Identify the blood parasite species.
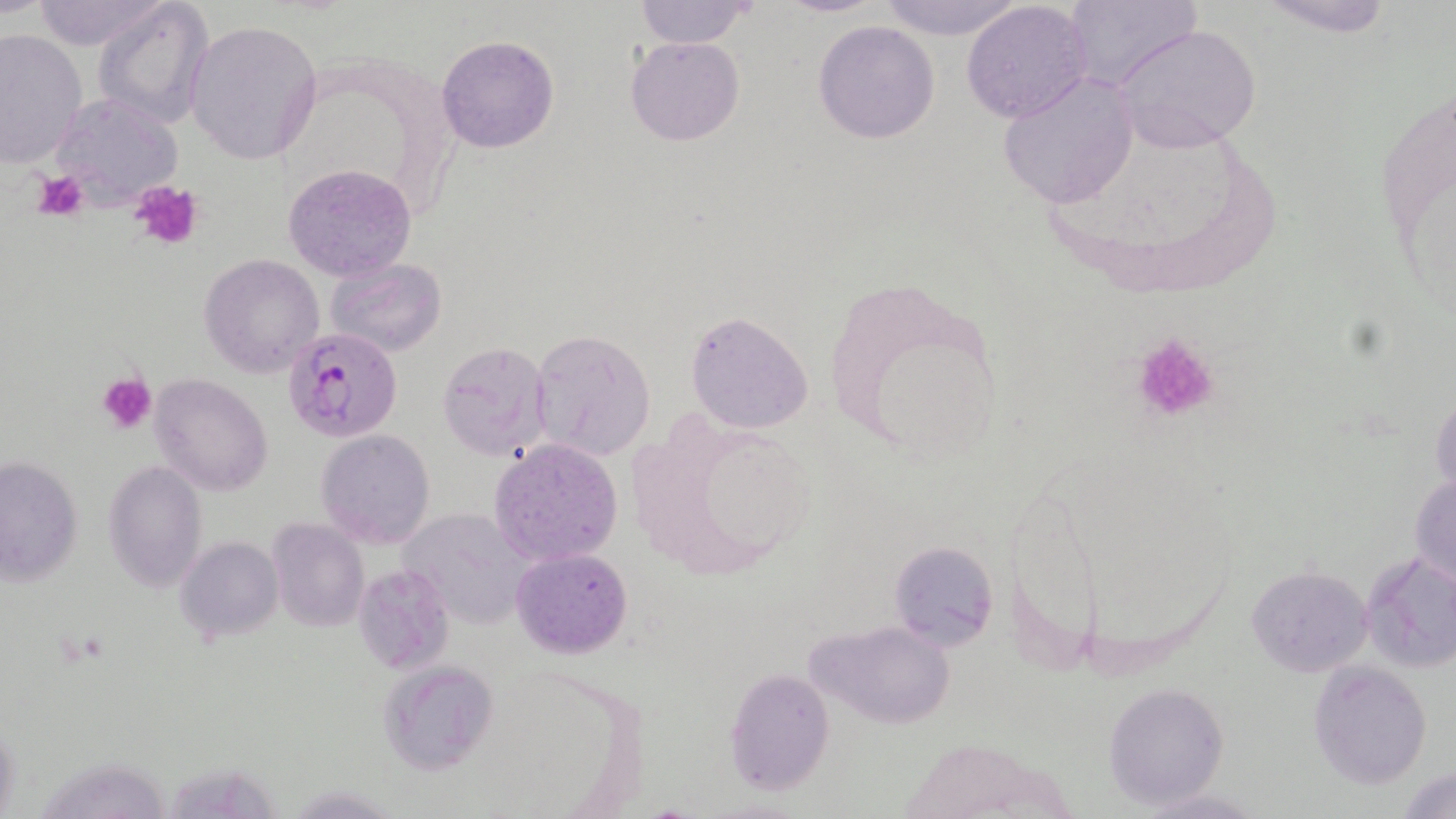

Plasmodium falciparum.

Summary:
  - Coordinate format: approximate bounding boxes as [x1, y1, x2, y2] in pixels
  - Platelet locations: [37, 174, 86, 219], [128, 181, 204, 250], [1128, 332, 1221, 424], [99, 373, 156, 433]
  - Plasmodium falciparum-infected red blood cell locations: [285, 329, 399, 441]
  - Uninfected red blood cell locations: [26, 0, 170, 51], [94, 0, 214, 129], [633, 0, 756, 48], [774, 0, 887, 17], [876, 0, 1025, 40], [1065, 0, 1202, 96], [1255, 0, 1398, 38], [961, 2, 1093, 120], [186, 18, 322, 165], [812, 19, 940, 144], [1114, 23, 1261, 152], [0, 28, 87, 171], [436, 33, 559, 154], [625, 37, 744, 146], [999, 74, 1138, 208], [1372, 74, 1455, 335], [57, 92, 188, 211], [284, 164, 416, 281], [200, 253, 324, 377], [325, 256, 447, 356], [821, 273, 1011, 462], [685, 311, 814, 434], [531, 328, 655, 462], [438, 341, 554, 463], [149, 375, 273, 494], [1430, 391, 1456, 505], [316, 429, 435, 547], [488, 438, 623, 567], [0, 455, 83, 588], [103, 461, 207, 592], [1410, 466, 1456, 592], [395, 506, 534, 629], [267, 520, 367, 634], [175, 536, 284, 644], [890, 544, 997, 650], [511, 548, 632, 657], [1360, 550, 1456, 674], [355, 562, 453, 675], [1245, 565, 1373, 677], [808, 618, 957, 729], [378, 658, 502, 774], [1307, 661, 1433, 788], [725, 668, 834, 793], [1104, 682, 1229, 809], [41, 749, 183, 818], [1398, 765, 1456, 819]
  - Preparation: thin blood smear
  - Image size: 1456×819 pixels
  - Stain: May-Grünwald-Giemsa
  - Field of view: one of a larger specimen
  - Magnification: 1000x
  - Modality: optical microscopy